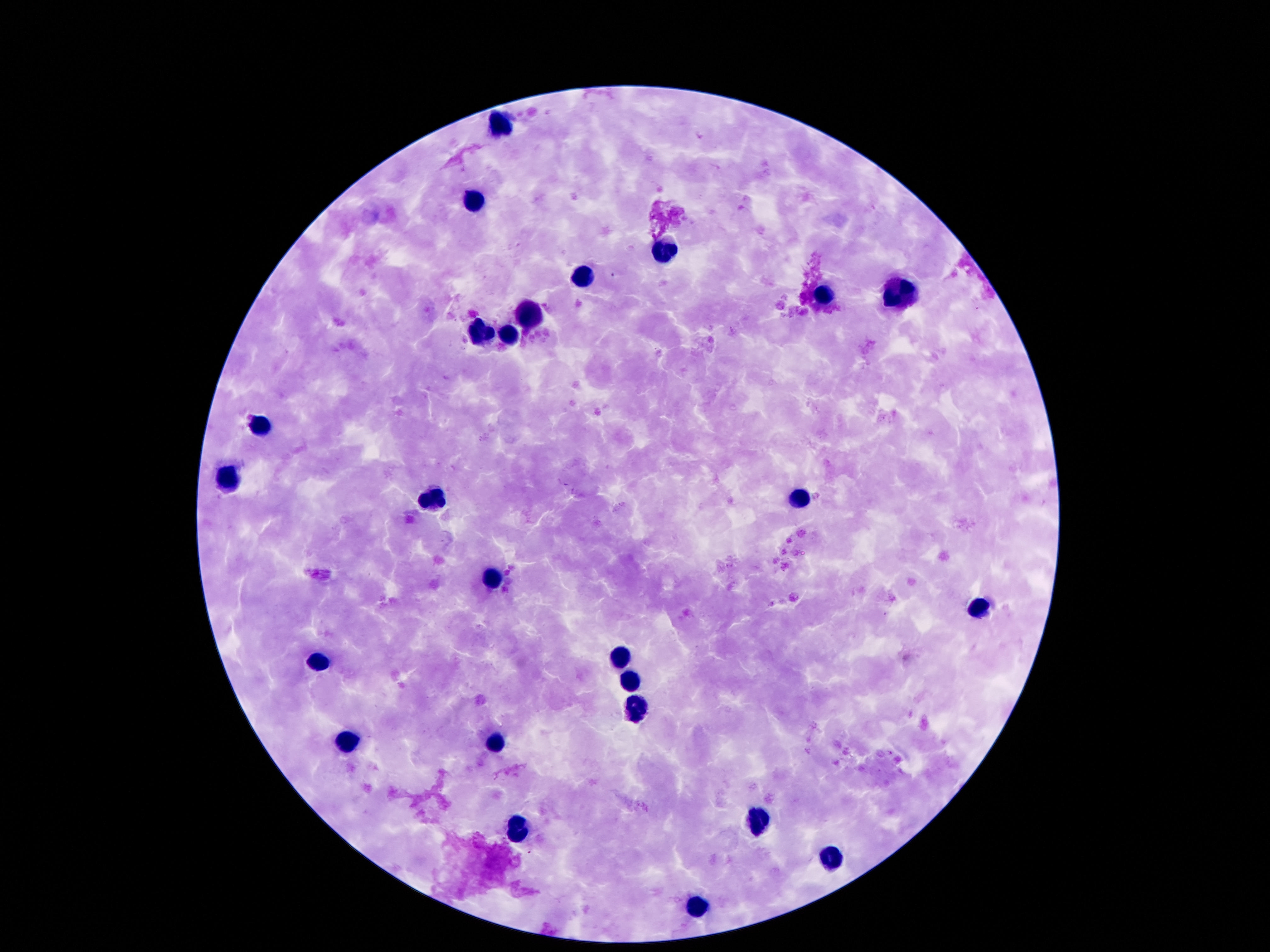
Approximate centers as {x, y} in pixels.
Summary:
  - Leukocyte locations: {500, 128}, {474, 202}, {664, 249}, {586, 274}, {905, 293}, {823, 297}, {530, 310}, {481, 333}, {511, 333}, {261, 424}, {233, 482}, {433, 495}, {800, 496}, {490, 575}, {980, 609}, {619, 658}, {317, 661}, {632, 682}, {634, 706}, {494, 742}, {347, 747}, {757, 824}, {515, 831}, {828, 861}, {696, 910}
  - Preparation: thick blood film
  - Stain: Giemsa
  - Field of view: one from this slide
  - Capture: smartphone camera through the microscope eyepiece
  - Image size: 1270×952 pixels
  - Patient malaria status: uninfected
  - Magnification: 100x